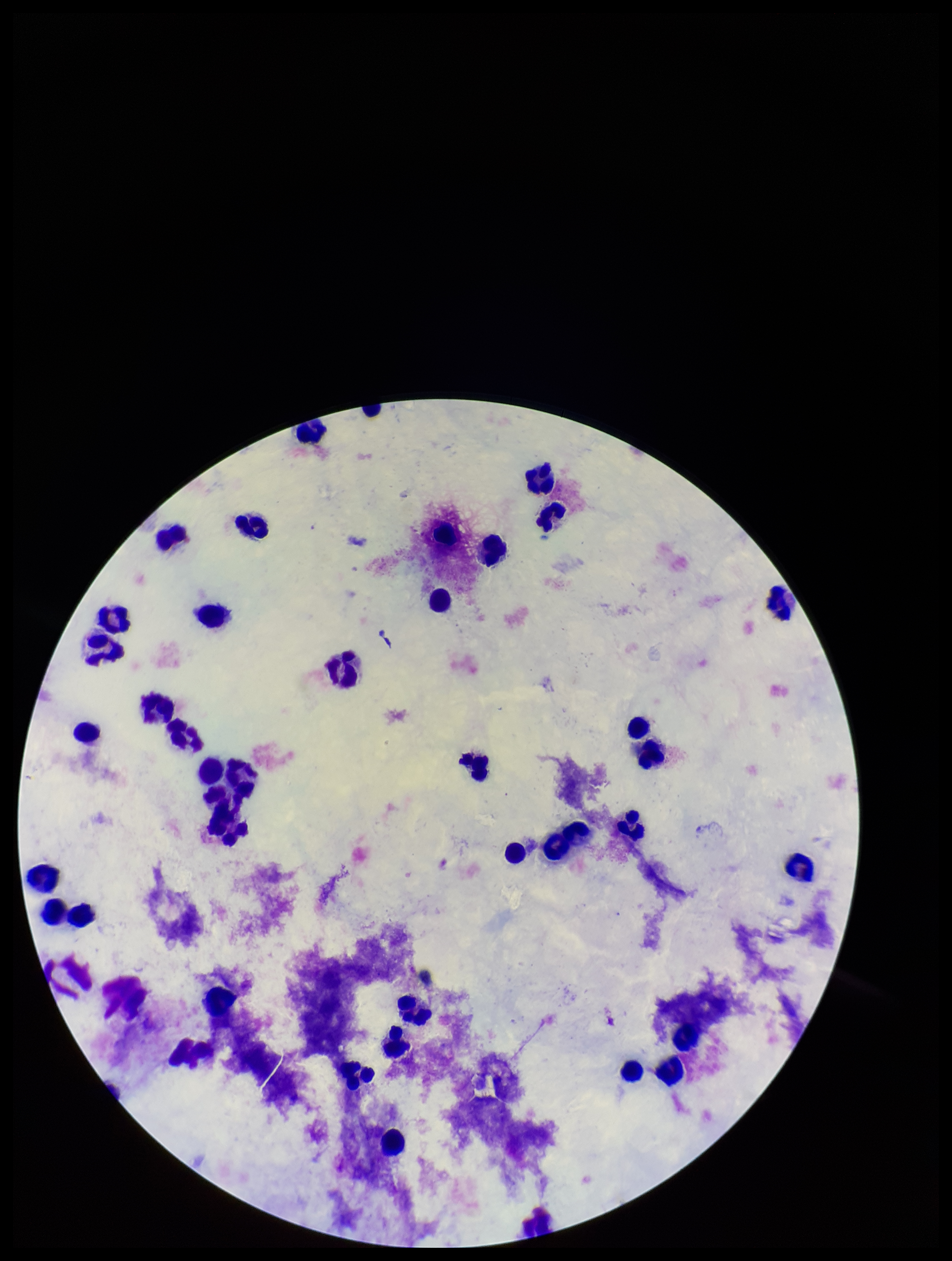
stain: Giemsa
image_size: 952×1261 pixels
preparation: thick smear
leukocyte_count: 38
plasmodium_parasites: none identified
parasite_count: 0
patient_malaria_status: negative
capture: smartphone photograph through the microscope eyepiece
field_of_view: one from this slide